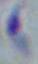
Summary:
  - Identification: Toxoplasma gondii
  - Modality: photomicrograph
  - Magnification: 1000x